Identify the blood parasite species.
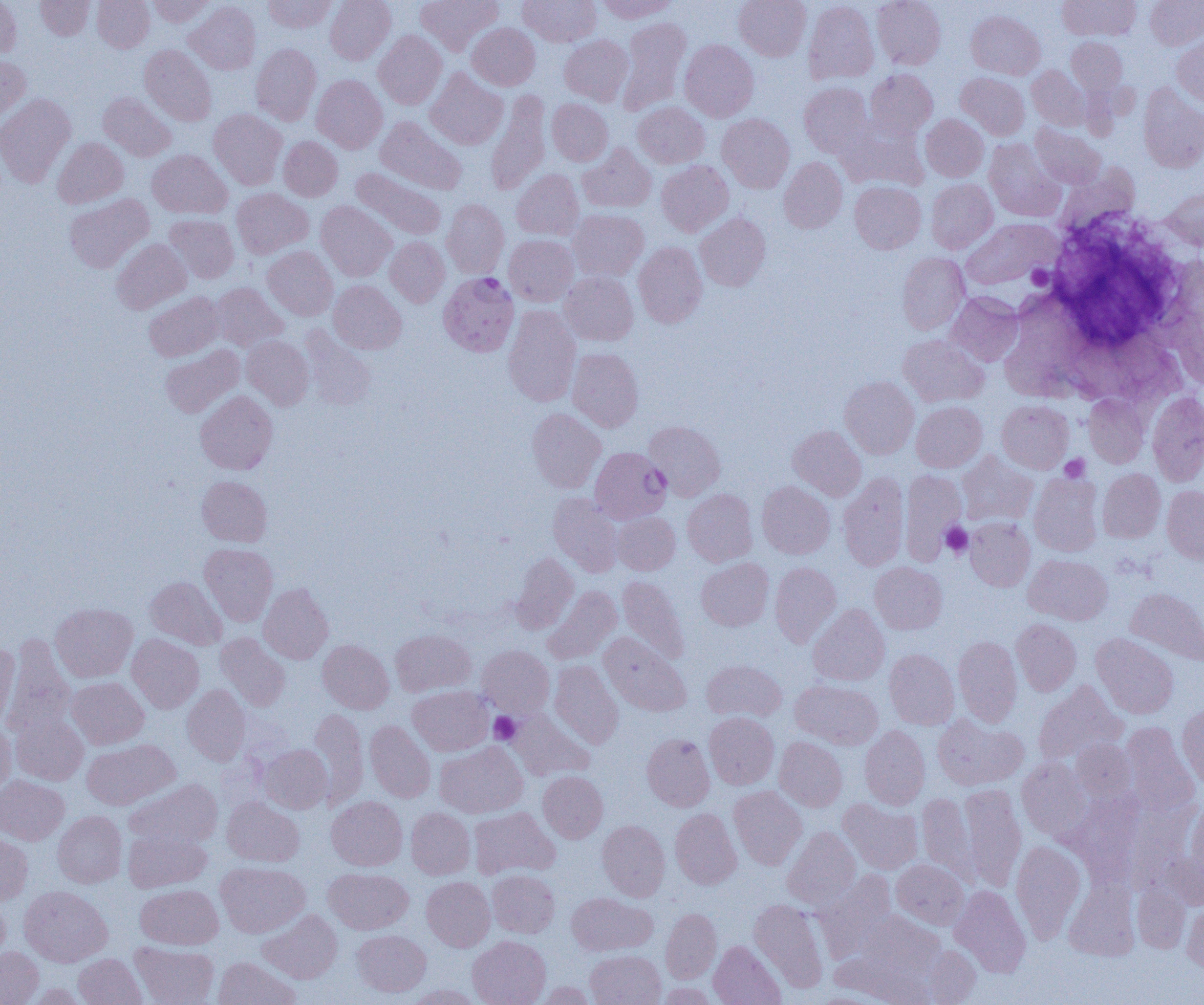

Plasmodium falciparum.

Approximate bounding boxes as (x1, y1, x2, y2) in pixels. Platelet locations: (1027, 265, 1054, 289), (1060, 455, 1090, 482), (941, 522, 973, 558), (489, 712, 522, 745). Plasmodium falciparum-infected red blood cell locations: (439, 272, 519, 357), (590, 446, 671, 524). Uninfected red blood cell locations: (0, 0, 21, 58), (36, 0, 95, 39), (92, 0, 154, 52), (147, 0, 216, 27), (263, 0, 336, 33), (325, 0, 395, 65), (416, 0, 502, 54), (518, 0, 601, 47), (596, 0, 678, 22), (733, 0, 811, 61), (872, 0, 946, 69), (1058, 0, 1140, 41), (1145, 0, 1204, 49), (184, 1, 261, 75), (804, 1, 879, 85), (967, 11, 1044, 79), (617, 17, 691, 115), (467, 23, 540, 90), (374, 31, 446, 109), (559, 34, 634, 106), (1172, 36, 1204, 107), (1066, 37, 1127, 98), (680, 39, 759, 121), (251, 43, 321, 126), (139, 45, 216, 126), (0, 56, 31, 125), (1027, 65, 1091, 130), (425, 68, 508, 150), (865, 69, 937, 139), (956, 72, 1029, 140), (311, 75, 387, 153), (799, 82, 874, 158), (1138, 83, 1204, 172), (98, 91, 176, 161), (486, 91, 551, 195), (0, 93, 76, 187), (547, 99, 613, 165), (633, 102, 709, 168), (209, 108, 287, 189), (717, 114, 795, 193), (921, 114, 988, 181), (375, 116, 466, 195), (838, 121, 928, 190), (1031, 124, 1106, 189), (279, 136, 343, 201), (53, 138, 128, 208), (984, 139, 1065, 221), (578, 143, 656, 213), (148, 150, 232, 218), (778, 157, 847, 233), (656, 160, 733, 236), (1057, 164, 1138, 235), (351, 167, 446, 240), (512, 169, 584, 240), (926, 179, 997, 253), (850, 181, 926, 254), (232, 188, 313, 259), (1161, 188, 1204, 250), (64, 194, 153, 273), (442, 199, 509, 279), (316, 201, 396, 280), (567, 209, 648, 282), (695, 212, 771, 291), (165, 214, 239, 283), (961, 219, 1059, 290), (504, 234, 578, 306), (385, 237, 449, 307), (111, 238, 191, 313), (634, 241, 707, 327), (262, 246, 338, 320), (897, 252, 970, 334), (559, 271, 638, 346), (329, 280, 406, 354), (210, 283, 288, 352), (144, 292, 223, 362), (946, 292, 1023, 366), (503, 306, 581, 407), (300, 327, 377, 409), (899, 334, 989, 407), (242, 335, 313, 410), (160, 345, 244, 418), (567, 348, 644, 432), (840, 377, 919, 459), (195, 391, 277, 474), (1147, 391, 1204, 486), (1084, 394, 1149, 467), (997, 400, 1073, 473), (911, 401, 987, 472), (527, 408, 606, 493), (644, 420, 725, 501), (788, 425, 866, 501), (956, 451, 1039, 526), (1097, 468, 1166, 543), (900, 469, 966, 564), (838, 473, 909, 571), (1029, 473, 1104, 557), (197, 476, 272, 546), (757, 482, 835, 559), (1162, 485, 1204, 564), (683, 488, 757, 566), (548, 492, 623, 576), (613, 511, 680, 575), (965, 517, 1035, 591), (200, 543, 278, 625), (511, 552, 579, 633), (1023, 554, 1113, 625), (696, 557, 774, 631), (869, 562, 947, 634), (770, 563, 841, 647), (146, 576, 227, 650), (618, 576, 689, 664), (259, 583, 333, 664), (543, 586, 621, 664), (1126, 587, 1204, 665), (51, 602, 138, 682), (808, 604, 890, 686), (1011, 618, 1081, 696), (391, 629, 475, 696), (215, 633, 290, 711), (599, 633, 691, 715), (1091, 633, 1178, 718), (127, 634, 204, 713), (3, 635, 75, 739), (953, 636, 1022, 726), (318, 639, 393, 713), (0, 643, 19, 727), (477, 646, 554, 717), (884, 648, 959, 729), (549, 660, 624, 749), (702, 660, 786, 722), (67, 677, 148, 749), (790, 680, 883, 749), (1033, 681, 1127, 765), (182, 684, 250, 766), (408, 686, 493, 755), (1178, 705, 1204, 789), (309, 708, 368, 807), (506, 710, 594, 781), (11, 712, 88, 785), (704, 713, 779, 789), (933, 713, 1028, 790), (365, 720, 435, 802), (0, 721, 15, 796), (1121, 723, 1199, 815), (860, 725, 930, 809), (642, 733, 714, 811), (774, 737, 847, 811), (82, 739, 179, 809), (1071, 739, 1136, 804), (434, 741, 528, 818), (260, 744, 333, 813), (1017, 757, 1093, 841), (538, 771, 608, 842), (0, 776, 69, 845), (124, 779, 222, 847), (959, 784, 1026, 891), (729, 785, 807, 869), (1068, 791, 1144, 884), (917, 793, 977, 882), (222, 796, 304, 866), (327, 796, 407, 870), (1132, 797, 1203, 892), (838, 798, 923, 874), (1186, 800, 1204, 886), (468, 807, 559, 879), (406, 808, 475, 879), (670, 808, 742, 889), (53, 811, 126, 887), (597, 815, 741, 893), (597, 820, 670, 901), (782, 827, 861, 908), (123, 828, 211, 892), (0, 833, 32, 904), (1010, 841, 1086, 942), (892, 859, 969, 929), (216, 862, 310, 937), (324, 868, 413, 934), (488, 870, 559, 937), (815, 871, 896, 956), (422, 876, 495, 951), (1065, 881, 1139, 960), (136, 884, 223, 949), (1132, 884, 1191, 952), (20, 885, 113, 967), (950, 885, 1031, 977), (566, 892, 657, 956), (0, 894, 10, 967), (749, 899, 828, 991), (1182, 902, 1204, 974), (661, 908, 721, 983), (258, 910, 342, 983), (852, 911, 944, 980), (352, 929, 431, 997), (467, 935, 551, 1005), (708, 941, 785, 1005), (130, 942, 218, 1005), (922, 945, 981, 1004), (0, 946, 43, 1005), (585, 950, 665, 1005), (73, 953, 146, 1005), (213, 956, 300, 1005), (536, 981, 597, 1005), (656, 982, 718, 1005), (407, 984, 483, 1005). Single field of view. 1000x magnification. Light microscopy. Image is 1204×1005 pixels. Thin blood smear.